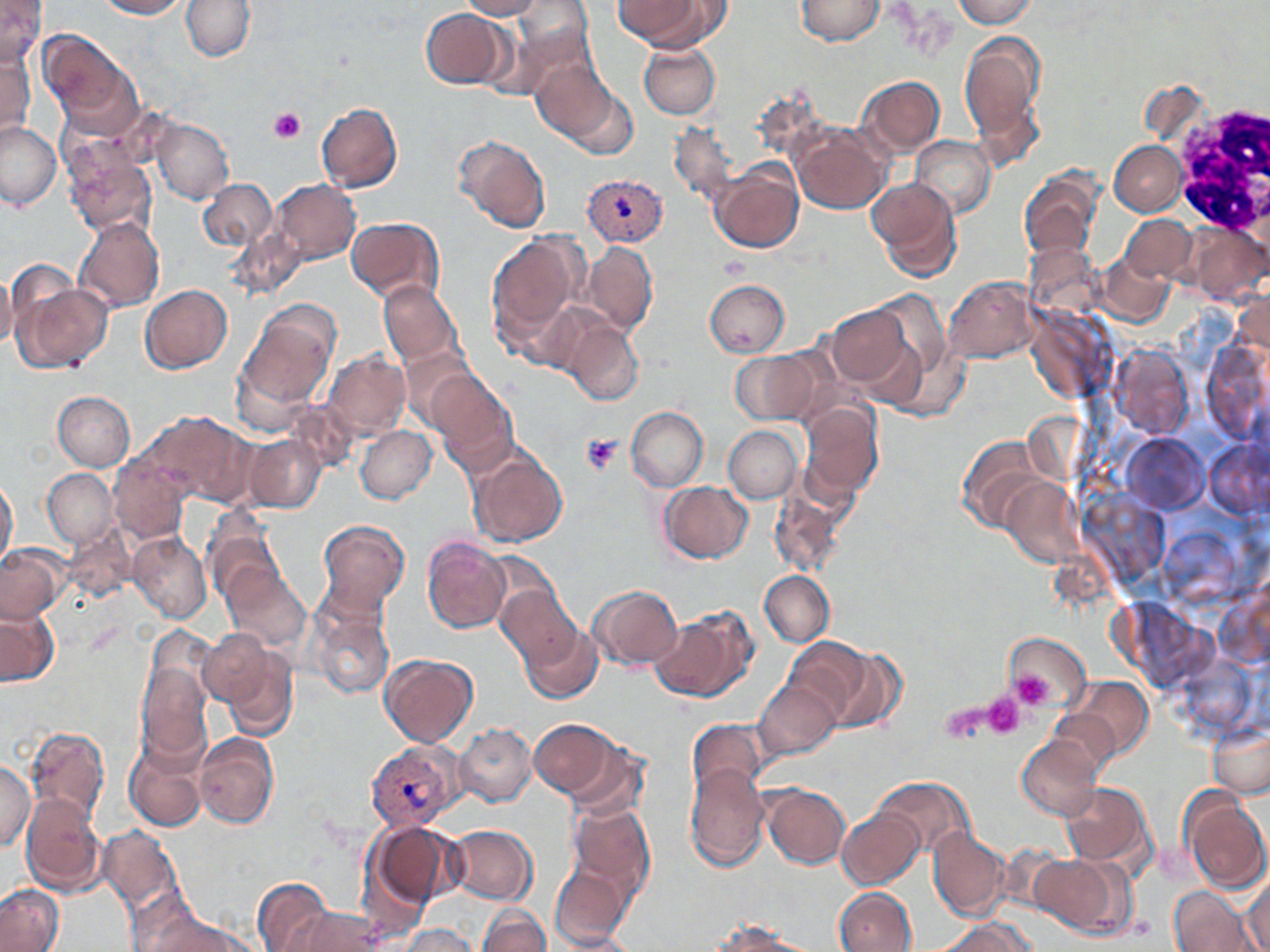

Approximate bounding boxes as (x1,y1)-(x2,y2) corner pairs in pixels. Plasmodium vivax-infected red blood cell locations: (582,173)-(667,247), (366,740)-(467,830). White blood cell locations: (1169,99)-(1270,244). Platelet locations: (269,106)-(305,143), (580,432)-(622,475), (1009,672)-(1056,709), (983,692)-(1025,739), (943,700)-(993,743). Uninfected red blood cell locations: (0,0)-(46,68), (96,0)-(186,19), (181,0)-(254,61), (457,0)-(544,19), (613,0)-(717,49), (795,0)-(884,46), (953,0)-(1036,28), (511,1)-(595,79), (420,8)-(510,89), (38,32)-(136,129), (959,33)-(1045,143), (638,43)-(719,120), (1,51)-(34,139), (531,59)-(622,144), (857,76)-(943,156), (557,78)-(642,161), (749,90)-(827,165), (316,102)-(403,193), (153,119)-(234,204), (0,121)-(62,209), (669,121)-(738,206), (792,122)-(889,214), (454,135)-(550,233), (910,135)-(995,218), (1110,140)-(1188,215), (65,151)-(155,236), (711,164)-(805,253), (1019,171)-(1101,264), (868,178)-(963,282), (198,180)-(276,252), (273,180)-(360,263), (1122,216)-(1196,282), (74,217)-(163,313), (346,217)-(442,302), (1187,221)-(1268,304), (231,226)-(307,300), (486,233)-(581,340), (584,242)-(657,335), (1098,252)-(1174,328), (5,260)-(72,339), (0,269)-(17,349), (945,277)-(1036,364), (705,278)-(790,356), (379,280)-(460,366), (16,283)-(111,372), (140,285)-(233,373), (1233,289)-(1270,362), (826,304)-(914,389), (239,307)-(336,408), (563,319)-(643,406), (1202,339)-(1268,445), (1108,343)-(1193,438), (399,347)-(476,428), (732,350)-(824,424), (324,351)-(409,437), (428,371)-(517,468), (53,392)-(134,471), (287,400)-(361,472), (799,401)-(883,498), (626,406)-(708,491), (148,411)-(252,506), (724,426)-(802,503), (355,427)-(436,504), (1121,432)-(1208,514), (245,434)-(327,513), (955,435)-(1048,534), (1205,441)-(1270,518), (466,449)-(567,548), (110,457)-(191,544), (43,469)-(117,547), (1000,478)-(1083,566), (0,479)-(18,568), (659,481)-(752,562), (769,484)-(850,578), (201,516)-(284,605), (317,521)-(409,614), (65,523)-(137,603), (128,533)-(211,623), (422,536)-(510,634), (0,544)-(65,624), (483,553)-(561,627), (222,567)-(311,652), (759,570)-(834,647), (588,585)-(682,670), (497,586)-(582,668), (0,606)-(59,685), (310,609)-(393,699), (652,610)-(753,701), (520,622)-(602,704), (197,627)-(275,708), (1003,632)-(1090,713), (784,638)-(872,722), (219,645)-(299,742), (828,648)-(908,734), (379,654)-(478,746), (137,661)-(212,764), (1069,676)-(1152,757), (754,680)-(839,759), (1048,709)-(1121,777), (686,718)-(768,802), (529,720)-(621,800), (454,724)-(536,805), (1209,725)-(1270,799), (25,726)-(110,827), (194,732)-(277,829), (1017,736)-(1100,822), (124,737)-(208,832), (563,742)-(649,823), (0,761)-(36,850), (683,761)-(769,870), (872,776)-(974,860), (1060,784)-(1155,867), (760,785)-(850,869), (1179,789)-(1269,894), (21,795)-(106,896), (568,803)-(654,897), (836,807)-(925,890), (366,821)-(463,912), (97,825)-(184,915), (446,825)-(538,904), (928,827)-(1010,921), (993,842)-(1069,915), (1033,853)-(1134,939), (549,863)-(633,949), (1244,874)-(1270,952), (252,878)-(333,951), (0,884)-(65,951), (1169,886)-(1256,952), (836,888)-(917,951), (477,905)-(548,952), (136,907)-(252,952), (285,907)-(384,952), (938,918)-(1034,952), (708,923)-(811,951), (399,924)-(479,952), (554,932)-(636,951). Slide-level diagnosis: Plasmodium vivax. One field of a larger specimen. 1000x magnification. Image is 1270×952 pixels. May-Grünwald-Giemsa-stained preparation. Light microscopy. Thin blood smear.